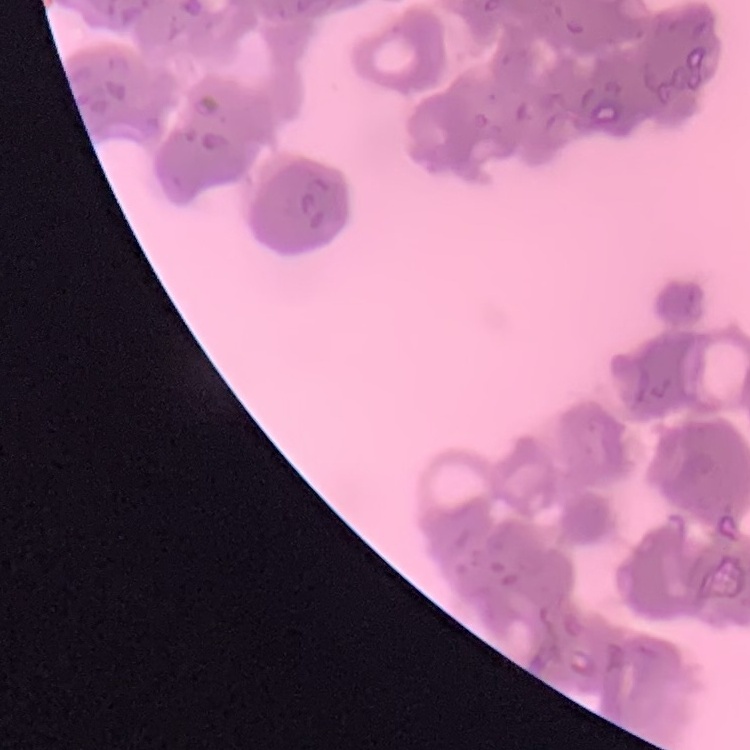
red blood cell morphology = rouleaux formation
stain = Field's or Giemsa
preparation = thin blood film
image type = one tile cut from a larger photomicrograph